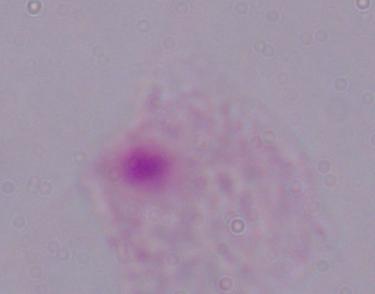

Summary:
  - Modality: photomicrograph
  - Magnification: 1000x
  - Identification: trichomonad